Report the malaria status of this cell.
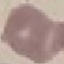
It is uninfected.

Acquired by smartphone through the microscope eyepiece. Thin blood smear. Giemsa-stained preparation. Automatically extracted cell patch, resized to 64 × 64 pixels.